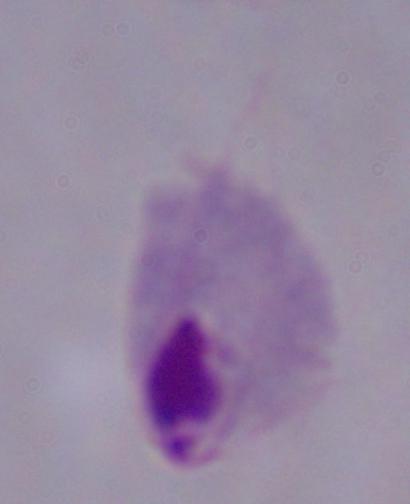
Micrograph. Captured at 1000x magnification. A trichomonad is seen.